State which parasite is depicted.
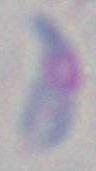

Toxoplasma gondii.

magnification: 1000x
modality: photomicrograph